Locate every blood parasite and identify its species.
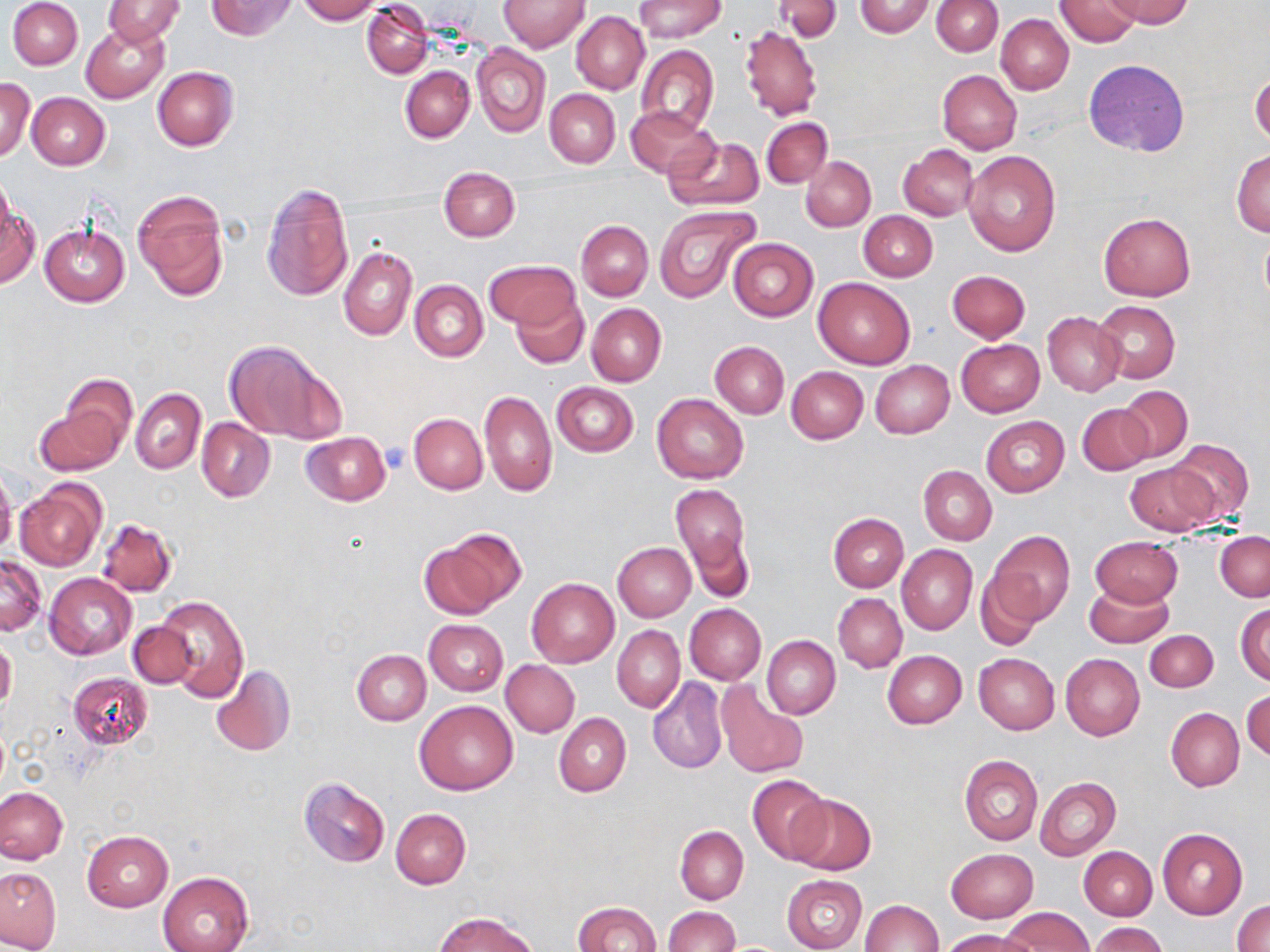

No blood parasites seen.

Summary:
  - Coordinate format: approximate bounding boxes as [x1, y1, x2, y2] in pixels
  - Uninfected red blood cell locations: [7, 0, 83, 70], [103, 0, 185, 46], [206, 0, 297, 40], [296, 0, 380, 23], [498, 0, 589, 51], [634, 0, 726, 43], [775, 0, 843, 40], [1104, 0, 1193, 27], [853, 1, 934, 37], [931, 1, 1002, 55], [1055, 1, 1141, 48], [363, 2, 433, 77], [572, 11, 649, 94], [996, 14, 1074, 94], [81, 21, 170, 103], [739, 23, 823, 122], [473, 45, 549, 136], [636, 46, 718, 137], [1084, 59, 1190, 156], [152, 66, 238, 151], [401, 66, 475, 141], [938, 70, 1022, 155], [1250, 70, 1269, 148], [1, 77, 35, 161], [545, 89, 620, 168], [27, 93, 109, 170], [625, 106, 717, 179], [761, 117, 833, 188], [665, 134, 764, 212], [899, 144, 978, 221], [963, 150, 1060, 257], [1231, 150, 1270, 237], [801, 156, 876, 231], [439, 173, 520, 239], [261, 182, 354, 303], [134, 191, 229, 301], [1, 201, 38, 287], [653, 205, 758, 301], [859, 211, 937, 282], [1098, 213, 1195, 302], [576, 220, 653, 300], [40, 224, 128, 307], [1259, 227, 1270, 313], [727, 238, 818, 321], [338, 245, 417, 340], [485, 260, 578, 329], [948, 270, 1030, 343], [812, 275, 916, 369], [410, 280, 488, 362], [510, 292, 590, 368], [1094, 301, 1180, 383], [586, 303, 667, 386], [1042, 311, 1125, 397], [957, 339, 1045, 417], [225, 340, 341, 442], [711, 341, 789, 418], [870, 360, 954, 438], [786, 366, 868, 444], [56, 374, 138, 454], [552, 381, 639, 457], [1118, 385, 1193, 462], [131, 388, 206, 475], [479, 389, 556, 496], [652, 394, 749, 483], [35, 404, 125, 476], [1077, 404, 1151, 474], [409, 413, 487, 494], [981, 416, 1069, 496], [197, 418, 274, 501], [300, 432, 390, 506], [1168, 438, 1255, 522], [1124, 462, 1218, 536], [919, 466, 996, 544], [0, 469, 17, 557], [15, 480, 106, 572], [670, 482, 751, 589], [828, 512, 908, 591], [96, 517, 177, 598], [423, 529, 524, 619], [989, 530, 1074, 625], [1216, 531, 1270, 601], [1091, 536, 1183, 608], [614, 543, 696, 621], [896, 545, 977, 634], [0, 556, 45, 635], [975, 571, 1045, 649], [45, 573, 137, 660], [527, 578, 619, 668], [1084, 582, 1174, 649], [833, 593, 906, 672], [155, 595, 249, 703], [1236, 603, 1270, 684], [685, 604, 766, 685], [422, 619, 507, 695], [128, 622, 198, 689], [612, 625, 684, 713], [1145, 631, 1217, 691], [763, 635, 840, 719], [0, 636, 17, 714], [352, 649, 431, 726], [883, 650, 966, 728], [1060, 653, 1144, 741], [973, 654, 1060, 734], [502, 660, 580, 737], [209, 663, 295, 757], [68, 671, 153, 752], [648, 677, 728, 774], [718, 684, 808, 779], [1243, 689, 1270, 764], [416, 700, 518, 795], [1165, 708, 1243, 791], [553, 713, 631, 798], [959, 755, 1042, 846], [747, 774, 831, 866], [298, 777, 391, 867], [1035, 777, 1121, 861], [0, 787, 68, 864], [786, 794, 876, 875], [391, 809, 470, 888], [675, 826, 748, 905], [1157, 828, 1248, 919], [83, 829, 173, 912], [1078, 845, 1157, 920], [946, 848, 1038, 923], [0, 867, 61, 951], [158, 872, 253, 952], [781, 874, 868, 952], [860, 899, 942, 952], [1232, 899, 1270, 952], [573, 901, 660, 952], [663, 906, 740, 952], [1001, 907, 1093, 952], [437, 912, 535, 952], [1090, 922, 1167, 952], [941, 930, 1036, 952]
  - Platelet locations: [381, 444, 414, 473]
  - Slide-level diagnosis: negative for blood parasites
  - Image size: 1270×952 pixels
  - Stain: May-Grünwald-Giemsa
  - Preparation: thin blood smear
  - Field of view: single
  - Modality: light microscopy
  - Magnification: 1000x